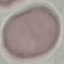

malaria status = uninfected
stain = Giemsa
capture = smartphone camera at the microscope eyepiece
image type = cell patch, automatically extracted from a larger field of view and resized to 64 × 64 pixels
preparation = thin blood film